Look for parasitized red blood cells.
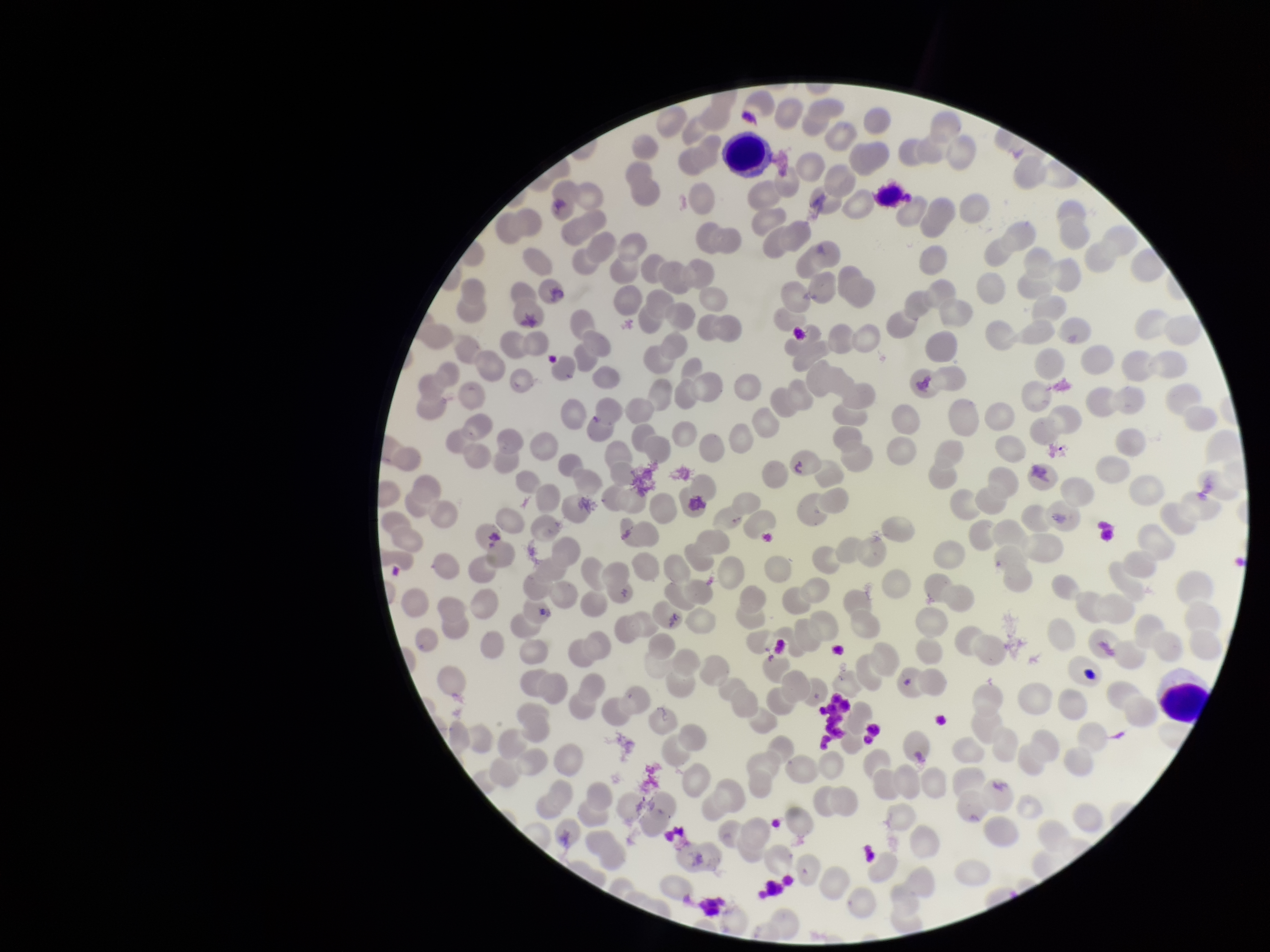

None seen.

Red blood cell count: 221. Image is 1270×952 pixels. Patient malaria status: negative. Preparation: thin smear. One field from this slide. Photographed through the microscope eyepiece with a smartphone camera. Giemsa stain. Parasitized red blood cell count: 0.